Identify the parasite.
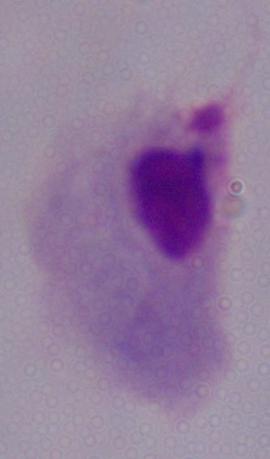

This is a trichomonad.

modality = photomicrograph
magnification = 1000x